State which parasite is depicted.
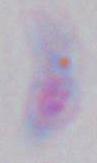

This is Toxoplasma gondii.

modality: photomicrograph
magnification: 1000x